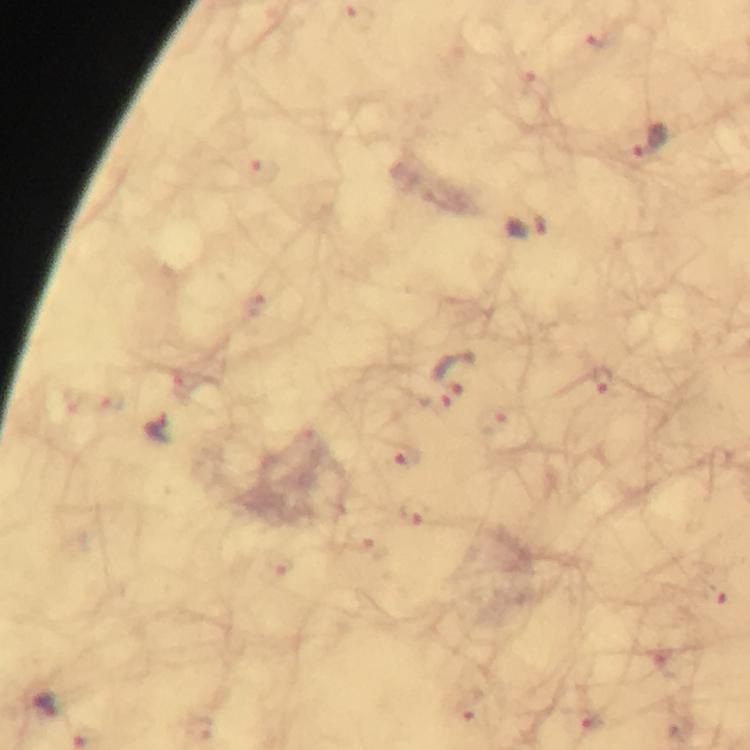
Approximate centers as {x, y} in pixels.
Summary:
  - Plasmodium parasite locations: {357, 17}, {597, 38}, {532, 88}, {651, 142}, {260, 171}, {527, 227}, {258, 306}, {456, 373}, {603, 381}, {185, 383}, {112, 400}, {73, 401}, {435, 405}, {494, 425}, {157, 427}, {310, 440}, {407, 455}, {416, 513}, {362, 541}, {284, 564}, {714, 594}, {656, 660}, {46, 704}, {471, 711}, {590, 724}, {202, 727}
  - Preparation: thick blood smear
  - Cropped from: a single field of view
  - Image size: 750×750 pixels
  - Magnification: 100x
  - Stain: Giemsa
  - Immersion oil: used
  - Capture: smartphone camera through the microscope
  - Context: from a diagnostic examination for malaria